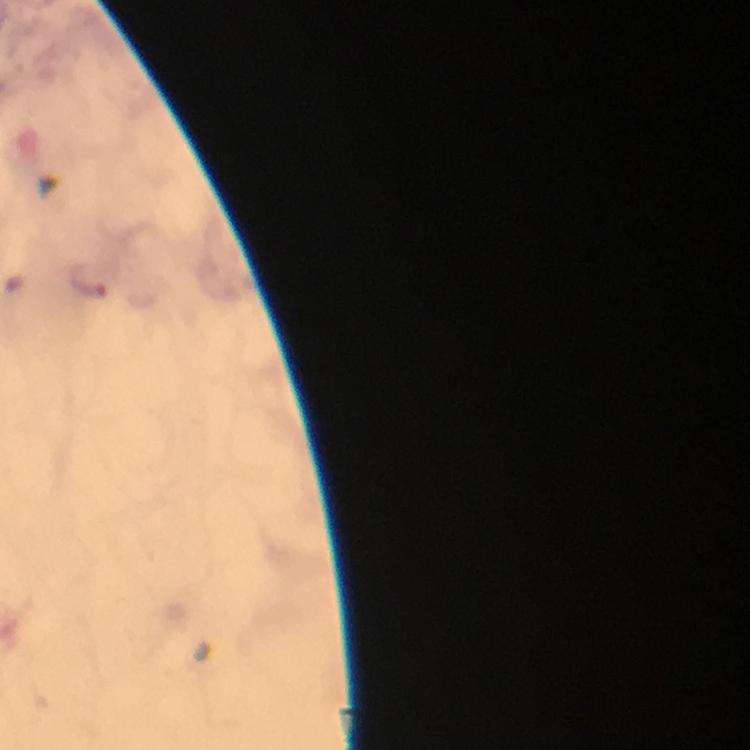
immersion oil = applied
preparation = thick blood film
capture = smartphone photograph through a microscope
context = from a malaria diagnostic workup
Plasmodium parasite locations = approximate centers as {x, y} in pixels: {89, 279}
stain = Giemsa
image size = 750×750 pixels
magnification = 100x
cropped from = a single field of view